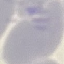
malaria_status: uninfected
stain: Giemsa
image_type: automatically extracted cell patch, resized to 64 × 64 pixels
capture: smartphone camera at the microscope eyepiece
preparation: thin smear